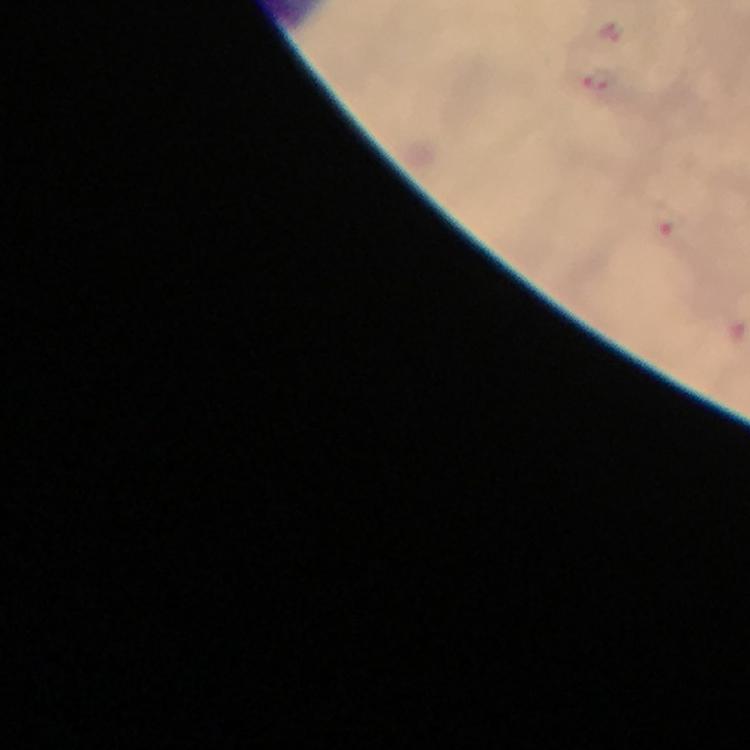

{
  "capture": "smartphone photograph through a microscope",
  "image_size": "750×750 pixels",
  "malaria_parasite_locations": "approximate object centers, in pixels from the top-left corner: (x=598, y=82), (x=672, y=224)",
  "stain": "Giemsa",
  "cropped_from": "one field of view",
  "magnification": "100x",
  "immersion_oil": "applied",
  "context": "from a malaria diagnostic workup",
  "preparation": "thick smear"
}